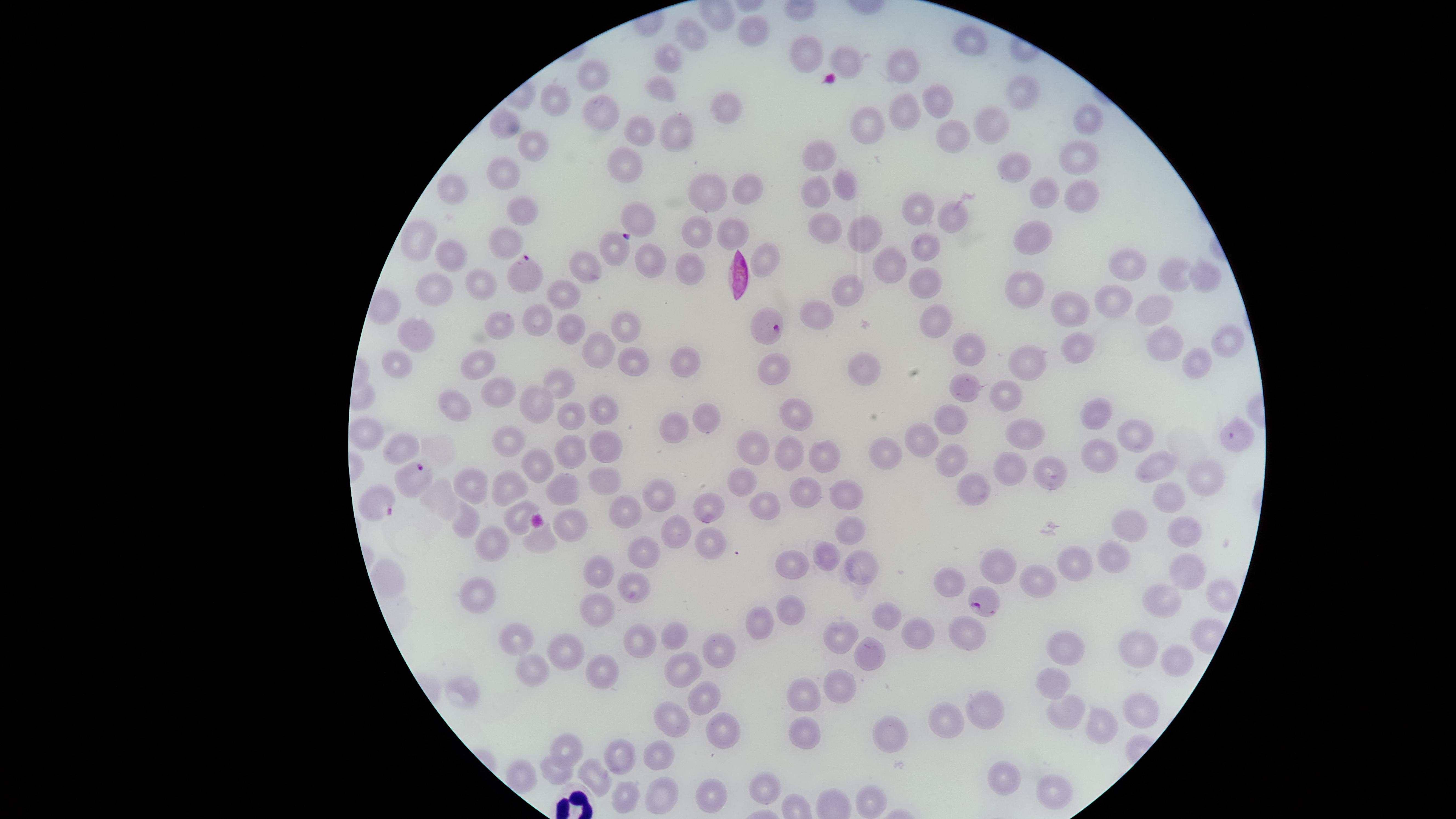

Approximate marker points as (x, y) in pixels.
Summary:
  - Parasitized RBCs: (617, 247), (524, 273), (767, 330), (1232, 435), (418, 472), (382, 503), (985, 600)
  - Uninfected RBCs: (751, 34), (689, 37), (971, 40), (809, 50), (669, 58), (845, 60), (900, 66), (590, 77), (663, 87), (1019, 91), (554, 98), (939, 101), (724, 106), (597, 112), (905, 112), (1083, 123), (503, 124), (993, 124), (636, 126), (865, 127), (679, 129), (950, 135), (533, 144), (1078, 155), (626, 156), (818, 159), (503, 166), (1008, 169), (846, 183), (451, 186), (745, 187), (704, 190), (814, 191), (1036, 191), (1078, 196), (917, 206), (520, 207), (951, 213), (639, 217), (829, 225), (733, 227), (694, 230), (863, 233), (417, 239), (1033, 240), (506, 244), (923, 246), (450, 252), (768, 255), (1128, 260), (654, 261), (584, 262), (888, 267), (685, 272), (1170, 274), (1203, 276), (928, 283), (434, 284), (481, 284), (1023, 289), (565, 292), (846, 292), (1109, 292), (1155, 307), (1060, 310), (809, 311), (936, 315), (540, 319), (626, 324), (500, 327), (571, 328), (418, 339), (1231, 344), (968, 347), (1162, 347), (1077, 348), (600, 351), (680, 358), (632, 359), (1197, 361), (401, 362), (1021, 362), (478, 363), (775, 372), (860, 372), (558, 379), (961, 389), (501, 391), (456, 397), (1002, 398), (536, 401), (610, 409), (569, 412), (796, 414), (1096, 415), (949, 418), (704, 421), (666, 429), (364, 431), (1029, 433), (1135, 436), (502, 440), (916, 440), (601, 444), (747, 447), (396, 449), (569, 449), (781, 449), (824, 451), (882, 451), (1099, 454), (952, 462), (1005, 465), (542, 467), (1157, 467), (1047, 473), (604, 479), (471, 481), (1199, 481), (739, 483), (508, 484), (808, 486), (978, 487), (561, 489), (844, 493), (660, 495), (1168, 497), (708, 505), (763, 507), (629, 511), (514, 518), (468, 521), (847, 523), (1135, 523), (568, 528), (1181, 528), (674, 529), (539, 540), (495, 543), (709, 550), (828, 552), (640, 554), (1114, 554), (998, 558), (794, 561), (1076, 566), (857, 570), (1188, 570), (597, 572), (390, 580), (1033, 582), (948, 584), (638, 591), (479, 593), (1216, 596), (1160, 601), (597, 605), (792, 606), (886, 612), (758, 626), (964, 636), (675, 637), (844, 637), (920, 637), (514, 639), (640, 644), (1064, 646), (717, 650), (1131, 650), (565, 651), (868, 655), (1175, 665), (603, 668), (683, 668), (534, 672), (1051, 684), (464, 687), (839, 692), (803, 693), (703, 699), (987, 702), (1132, 707), (1060, 711), (671, 718), (1102, 721), (942, 722), (803, 728), (724, 730), (892, 736), (563, 749), (660, 753), (623, 754), (551, 771), (597, 772), (518, 775), (1003, 777), (763, 786), (1055, 788), (660, 790), (704, 793), (622, 797), (866, 800)
  - Field of view: single
  - Presence: malaria parasites detected
  - Image size: 1456×819 pixels
  - Stain: Giemsa
  - Capture: smartphone photograph through the microscope eyepiece
  - Visible region: circular
  - Preparation: thin smear of blood
  - Species: Plasmodium falciparum